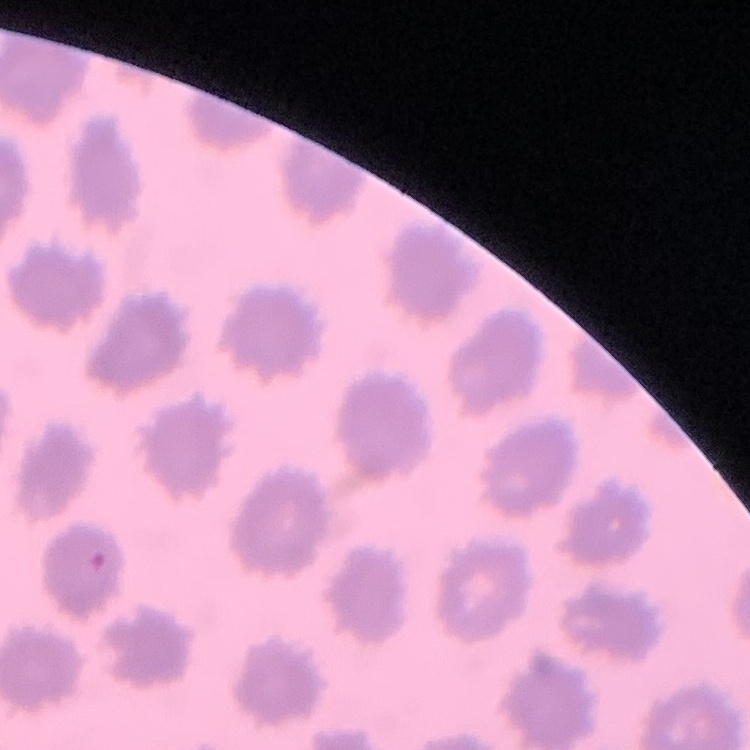

Summary:
  - Red blood cell morphology: no rouleaux formation
  - Stain: Field's or Giemsa
  - Image type: square crop of a larger photomicrograph
  - Preparation: thin blood smear